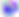
{
  "modality": "micrograph",
  "magnification": "400x",
  "identification": "Toxoplasma gondii"
}